Identify the blood parasite species.
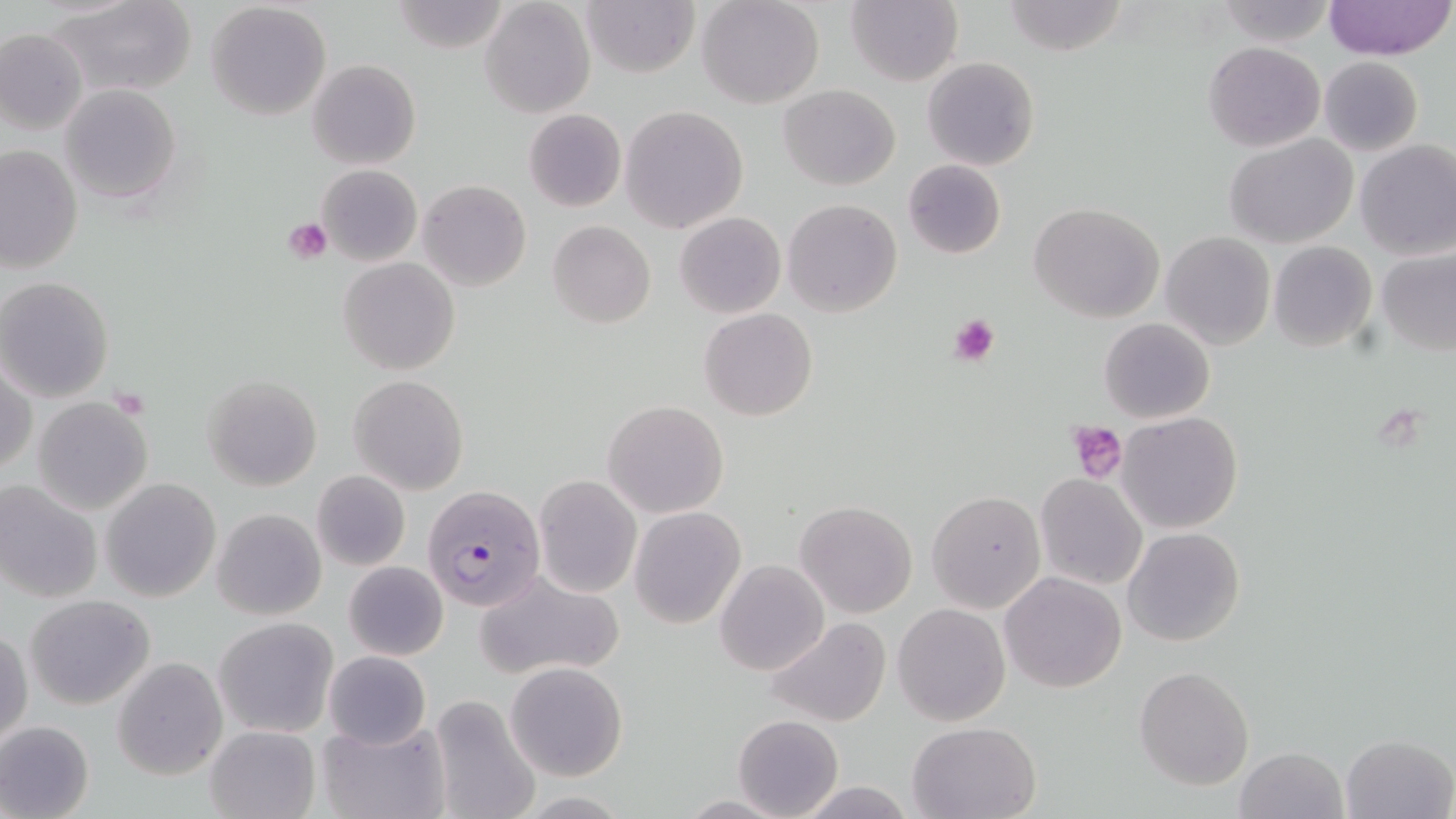
Plasmodium falciparum.

{
  "modality": "optical microscopy",
  "uninfected_red_blood_cell_locations": "approximate bounding boxes as (x1,y1)-(x2,y2) corner pairs in pixels: (50,0)-(197,98), (390,0)-(514,53), (581,0)-(701,77), (697,0)-(825,109), (846,0)-(962,87), (1002,0)-(1130,55), (1324,0)-(1456,61), (479,1)-(595,118), (1214,1)-(1335,46), (206,2)-(331,120), (0,27)-(87,136), (1204,41)-(1325,151), (922,56)-(1040,171), (1319,57)-(1423,155), (308,59)-(421,170), (60,83)-(181,203), (779,84)-(900,190), (621,106)-(748,233), (524,110)-(627,211), (1225,133)-(1359,248), (1355,140)-(1456,261), (0,145)-(83,277), (902,159)-(1006,260), (317,164)-(422,265), (418,180)-(531,293), (783,199)-(903,316), (1030,202)-(1167,323), (675,212)-(785,319), (547,220)-(656,329), (1160,231)-(1275,350), (1267,242)-(1377,351), (1377,250)-(1456,355), (338,257)-(460,376), (0,276)-(114,401), (699,307)-(817,421), (1099,318)-(1215,423), (1,361)-(36,475), (203,374)-(323,491), (348,374)-(469,494), (32,396)-(155,516), (603,401)-(729,517), (1117,411)-(1242,534), (311,469)-(411,572), (534,474)-(641,597), (1034,474)-(1147,590), (100,478)-(221,603), (0,479)-(103,604), (927,490)-(1045,612), (795,501)-(916,617), (629,507)-(745,627), (212,508)-(326,620), (1124,528)-(1245,647), (715,560)-(828,674), (344,561)-(449,661), (474,570)-(628,679), (999,572)-(1127,694), (26,595)-(155,709), (892,603)-(1010,727), (214,616)-(341,739), (764,616)-(892,727), (1,630)-(32,747), (325,651)-(430,748), (113,656)-(229,779), (505,662)-(627,781), (1134,666)-(1254,790), (426,695)-(541,819), (732,715)-(842,819), (318,716)-(448,819), (907,720)-(1042,817), (0,721)-(96,819), (206,724)-(320,819), (1341,733)-(1454,818), (1234,747)-(1348,819), (793,780)-(917,817)",
  "image_size": "1456×819 pixels",
  "stain": "May-Grünwald-Giemsa",
  "plasmodium_falciparum_infected_red_blood_cell_locations": "approximate bounding boxes as (x1,y1)-(x2,y2) corner pairs in pixels: (422,484)-(545,612)",
  "magnification": "1000x",
  "preparation": "thin blood smear",
  "platelet_locations": "approximate bounding boxes as (x1,y1)-(x2,y2) corner pairs in pixels: (284,218)-(333,264), (948,314)-(1001,367), (112,388)-(152,418), (1067,421)-(1128,482)",
  "field_of_view": "one of a larger specimen"
}